Locate and identify every blood parasite.
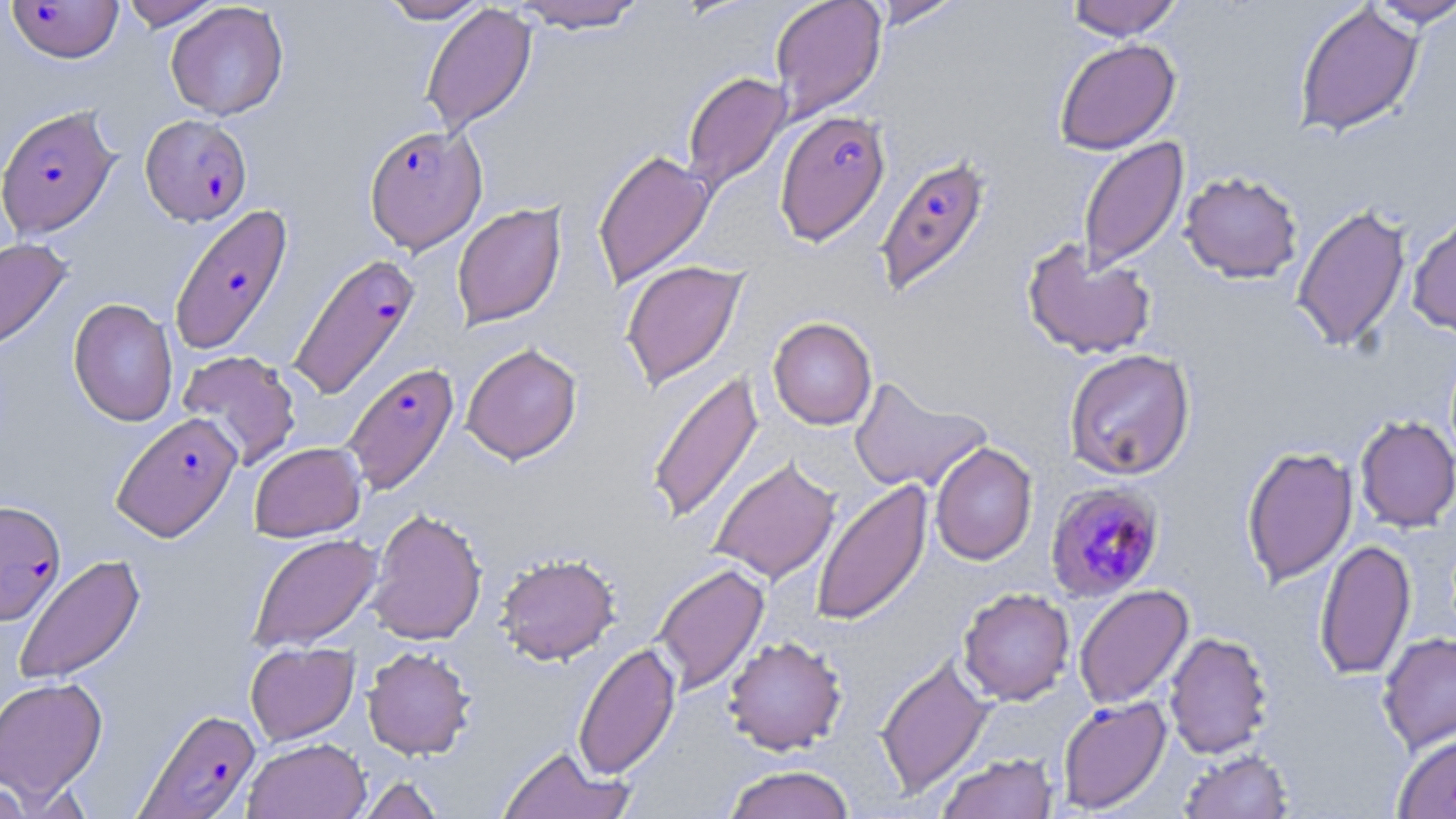
Approximate bounding boxes as [x1, y1, x2, y2] in pixels.
Plasmodium falciparum-infected red blood cells: [5, 1, 125, 63], [0, 104, 119, 239], [774, 109, 891, 246], [141, 114, 252, 226], [364, 124, 487, 253], [874, 153, 994, 298], [168, 203, 295, 356], [287, 252, 422, 401], [342, 363, 460, 495], [111, 411, 242, 542], [1045, 482, 1165, 603], [0, 499, 66, 625], [136, 707, 261, 818].
No Plasmodium ovale, Plasmodium malariae, Plasmodium vivax, Babesia divergens, or Trypanosoma brucei observed.

Uninfected red blood cell locations: [120, 0, 224, 30], [377, 0, 490, 24], [509, 0, 649, 32], [770, 0, 887, 122], [867, 0, 964, 29], [1065, 0, 1184, 40], [1363, 0, 1456, 27], [165, 2, 289, 120], [1293, 2, 1424, 137], [420, 3, 537, 138], [1053, 38, 1181, 155], [682, 71, 792, 194], [1077, 137, 1189, 273], [592, 149, 715, 290], [1179, 170, 1303, 283], [452, 202, 566, 330], [1291, 204, 1412, 352], [1407, 211, 1456, 337], [0, 237, 72, 354], [1021, 238, 1157, 360], [620, 260, 748, 391], [69, 298, 179, 427], [768, 317, 877, 430], [461, 342, 583, 464], [1063, 348, 1195, 480], [177, 350, 302, 471], [646, 369, 765, 525], [849, 376, 992, 495], [1355, 415, 1456, 532], [249, 442, 366, 542], [930, 442, 1038, 566], [1241, 445, 1357, 586], [709, 457, 841, 584], [811, 479, 933, 627], [366, 508, 487, 645], [247, 533, 382, 653], [1314, 539, 1416, 680], [495, 552, 621, 665], [13, 554, 146, 685], [653, 562, 770, 696], [1074, 584, 1194, 710], [958, 588, 1075, 705], [1164, 631, 1273, 759], [1377, 631, 1456, 755], [723, 635, 848, 755], [245, 642, 359, 745], [572, 642, 681, 780], [362, 645, 477, 760], [875, 653, 995, 798], [0, 676, 108, 802], [1057, 695, 1172, 814], [1391, 730, 1456, 819], [243, 737, 371, 819], [496, 745, 633, 819], [1179, 749, 1293, 819], [935, 752, 1059, 819], [722, 765, 856, 819], [359, 775, 445, 819], [0, 777, 33, 818]. Slide-level diagnosis: Plasmodium falciparum. Thin blood smear. 1000x magnification. Image is 1456×819 pixels. Light microscopy. May-Grünwald-Giemsa-stained preparation. Single field of view.